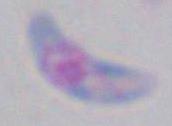
Summary:
  - Magnification: 1000x
  - Modality: micrograph
  - Identification: Toxoplasma gondii